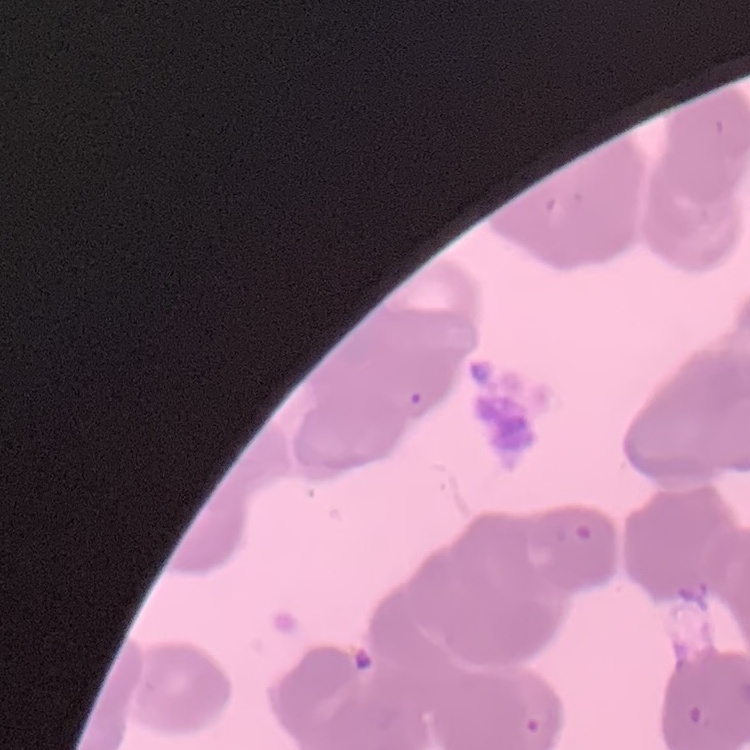

red blood cell morphology = rouleaux formation
image type = one tile cut from a larger photomicrograph
preparation = thin peripheral smear
stain = Field's or Giemsa